Outline each blood parasite and name the species.
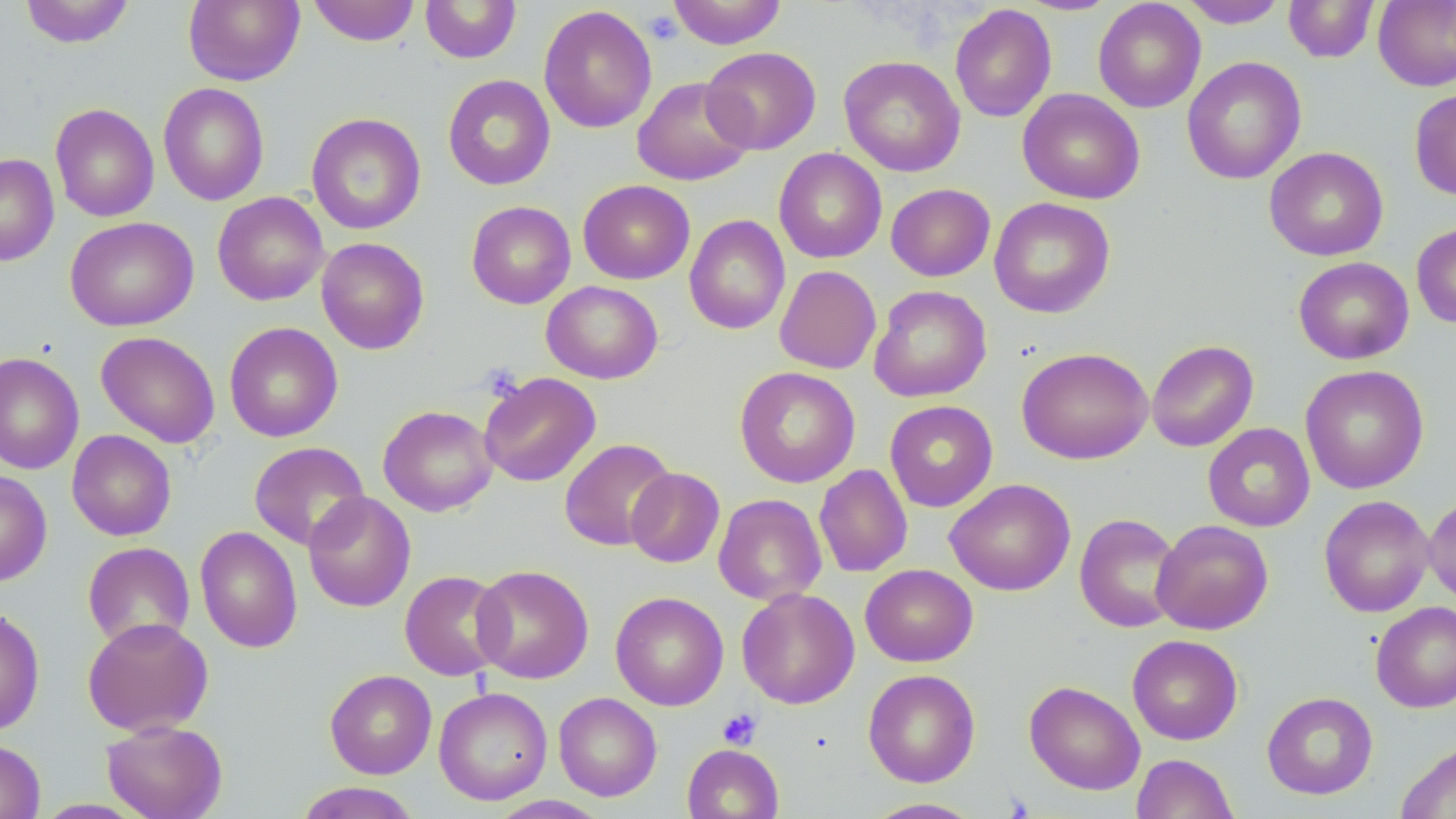

No blood parasites seen.

Approximate bounding boxes as named x1/y1/x2/y2 corners in pixels. Uninfected red blood cell locations: (x1=19, y1=0, x2=135, y2=48), (x1=183, y1=0, x2=304, y2=86), (x1=307, y1=0, x2=420, y2=46), (x1=666, y1=0, x2=787, y2=49), (x1=1015, y1=0, x2=1122, y2=15), (x1=1178, y1=0, x2=1289, y2=28), (x1=1284, y1=0, x2=1379, y2=63), (x1=420, y1=1, x2=521, y2=64), (x1=1093, y1=1, x2=1206, y2=113), (x1=1374, y1=1, x2=1456, y2=91), (x1=950, y1=4, x2=1057, y2=123), (x1=538, y1=5, x2=657, y2=133), (x1=701, y1=47, x2=821, y2=154), (x1=839, y1=55, x2=966, y2=177), (x1=1182, y1=56, x2=1307, y2=184), (x1=443, y1=74, x2=556, y2=191), (x1=632, y1=76, x2=755, y2=187), (x1=158, y1=83, x2=269, y2=206), (x1=1017, y1=88, x2=1145, y2=205), (x1=1409, y1=88, x2=1456, y2=200), (x1=50, y1=103, x2=159, y2=222), (x1=306, y1=112, x2=426, y2=235), (x1=1264, y1=147, x2=1388, y2=261), (x1=774, y1=148, x2=887, y2=263), (x1=0, y1=153, x2=59, y2=267), (x1=577, y1=180, x2=695, y2=284), (x1=886, y1=183, x2=995, y2=282), (x1=212, y1=192, x2=329, y2=306), (x1=988, y1=197, x2=1116, y2=318), (x1=466, y1=201, x2=576, y2=309), (x1=684, y1=214, x2=791, y2=335), (x1=64, y1=216, x2=198, y2=332), (x1=1411, y1=223, x2=1456, y2=328), (x1=316, y1=237, x2=429, y2=354), (x1=1293, y1=257, x2=1414, y2=364), (x1=774, y1=265, x2=881, y2=374), (x1=542, y1=281, x2=663, y2=384), (x1=868, y1=285, x2=992, y2=403), (x1=224, y1=322, x2=343, y2=442), (x1=95, y1=331, x2=220, y2=449), (x1=1146, y1=339, x2=1259, y2=452), (x1=1017, y1=347, x2=1154, y2=464), (x1=0, y1=352, x2=84, y2=475), (x1=1300, y1=364, x2=1429, y2=494), (x1=734, y1=366, x2=861, y2=488), (x1=478, y1=372, x2=601, y2=487), (x1=884, y1=400, x2=998, y2=512), (x1=378, y1=405, x2=498, y2=516), (x1=1203, y1=423, x2=1315, y2=532), (x1=67, y1=430, x2=176, y2=541), (x1=558, y1=438, x2=676, y2=551), (x1=248, y1=441, x2=370, y2=550), (x1=814, y1=464, x2=913, y2=577), (x1=626, y1=467, x2=725, y2=568), (x1=0, y1=469, x2=52, y2=586), (x1=945, y1=478, x2=1075, y2=596), (x1=303, y1=491, x2=416, y2=612), (x1=713, y1=493, x2=826, y2=606), (x1=1424, y1=493, x2=1456, y2=607), (x1=1318, y1=495, x2=1435, y2=617), (x1=1074, y1=513, x2=1183, y2=633), (x1=1151, y1=519, x2=1273, y2=634), (x1=195, y1=525, x2=303, y2=653), (x1=82, y1=542, x2=195, y2=650), (x1=471, y1=564, x2=594, y2=684), (x1=860, y1=564, x2=977, y2=667), (x1=399, y1=569, x2=510, y2=681), (x1=737, y1=587, x2=860, y2=709), (x1=610, y1=591, x2=728, y2=710), (x1=1370, y1=600, x2=1456, y2=713), (x1=0, y1=606, x2=45, y2=735), (x1=82, y1=616, x2=214, y2=737), (x1=1127, y1=634, x2=1244, y2=745), (x1=863, y1=668, x2=981, y2=787), (x1=325, y1=669, x2=437, y2=779), (x1=1024, y1=680, x2=1145, y2=795), (x1=434, y1=686, x2=553, y2=805), (x1=1262, y1=691, x2=1378, y2=799), (x1=554, y1=692, x2=662, y2=801), (x1=102, y1=719, x2=228, y2=819), (x1=0, y1=739, x2=46, y2=819), (x1=1395, y1=740, x2=1456, y2=819), (x1=682, y1=744, x2=783, y2=818), (x1=1131, y1=753, x2=1238, y2=819), (x1=293, y1=782, x2=424, y2=819), (x1=488, y1=795, x2=610, y2=819), (x1=861, y1=797, x2=986, y2=818). Platelet locations: (x1=644, y1=10, x2=683, y2=46), (x1=718, y1=708, x2=762, y2=750). Slide-level diagnosis: no evidence of blood parasites. Thin blood smear. Image is 1456×819 pixels. One field of a larger specimen. May-Grünwald-Giemsa-stained preparation. Optical microscopy. 1000x magnification.